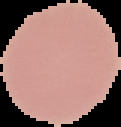

Summary:
  - Preparation: thin blood smear
  - Image size: 121×127 pixels
  - Image type: segmented cell region with the area outside set to black
  - Malaria status: uninfected